Locate every blood parasite and identify its species.
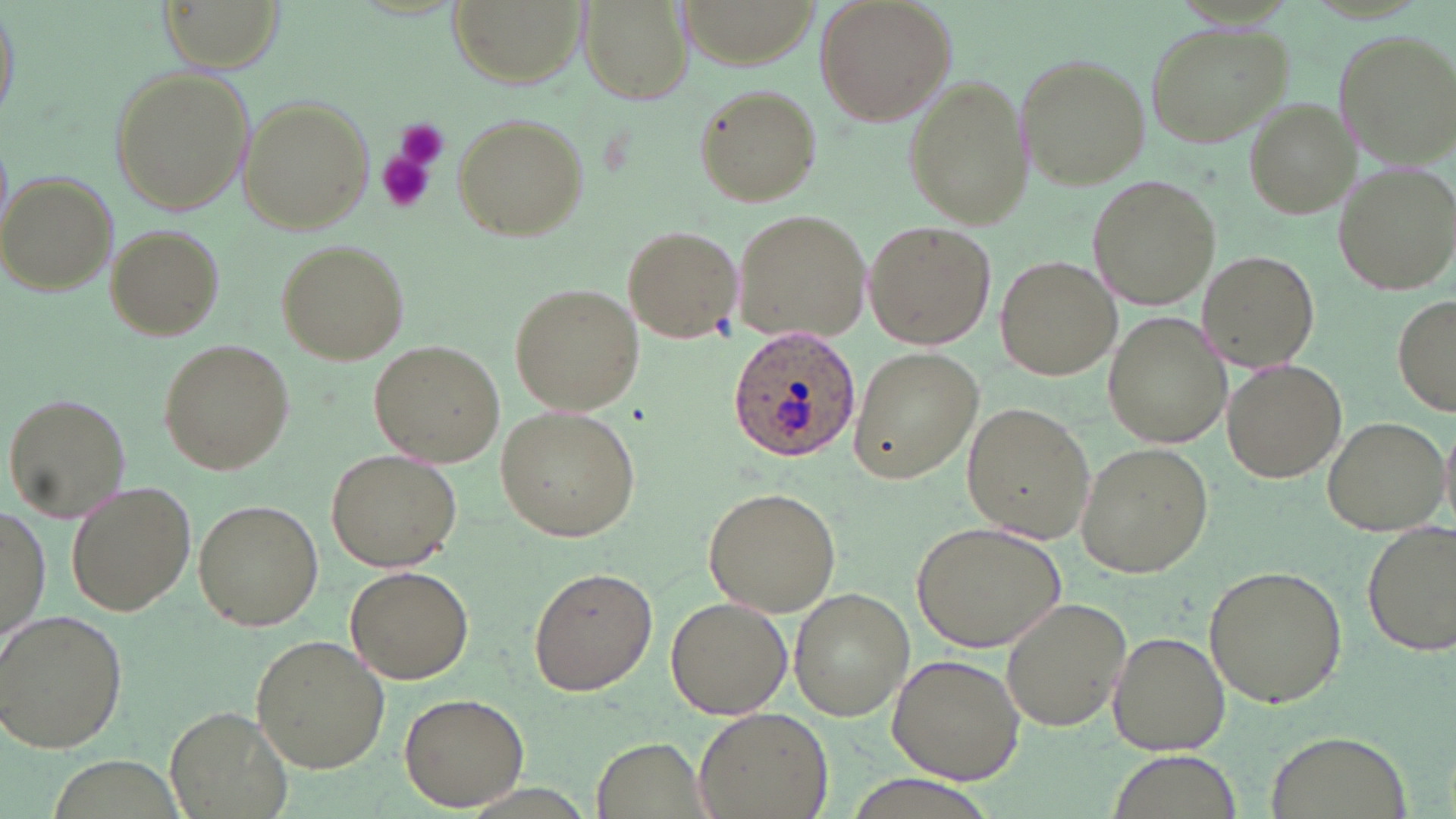
Approximate bounding boxes as [x1, y1, x2, y2] in pixels.
Plasmodium ovale-infected red blood cells: [725, 324, 860, 462].
No Plasmodium falciparum, Plasmodium malariae, Plasmodium vivax, Babesia divergens, or Trypanosoma brucei observed.

Uninfected red blood cell locations: [0, 0, 19, 132], [156, 0, 284, 72], [453, 0, 583, 87], [579, 0, 691, 106], [677, 0, 816, 66], [812, 0, 956, 126], [1145, 22, 1290, 150], [1334, 26, 1456, 164], [1015, 53, 1149, 188], [108, 64, 255, 217], [903, 75, 1030, 229], [692, 83, 823, 207], [237, 96, 373, 234], [1239, 99, 1354, 218], [451, 112, 590, 243], [1333, 162, 1455, 297], [1, 172, 119, 296], [1087, 175, 1217, 310], [731, 207, 873, 347], [863, 221, 994, 352], [622, 223, 742, 342], [105, 224, 222, 338], [275, 239, 409, 366], [1196, 249, 1320, 371], [996, 256, 1122, 381], [510, 282, 643, 415], [1391, 295, 1455, 416], [1103, 310, 1235, 447], [158, 339, 296, 477], [370, 340, 505, 467], [846, 348, 984, 484], [1221, 359, 1346, 483], [5, 393, 130, 521], [962, 400, 1098, 543], [496, 405, 641, 542], [1321, 415, 1448, 537], [1439, 421, 1456, 530], [1074, 442, 1212, 577], [326, 450, 459, 572], [67, 483, 196, 616], [702, 486, 841, 615], [195, 500, 323, 630], [0, 505, 47, 644], [914, 518, 1067, 652], [1361, 519, 1456, 655], [344, 562, 476, 684], [1203, 563, 1350, 709], [527, 565, 657, 695], [788, 589, 913, 721], [665, 595, 790, 719], [998, 597, 1132, 732], [0, 607, 130, 754], [1106, 631, 1230, 756], [249, 634, 389, 772], [887, 650, 1027, 784], [400, 690, 532, 811], [169, 705, 293, 819], [693, 707, 833, 818], [1262, 730, 1413, 819], [591, 738, 711, 818]. Platelet locations: [394, 118, 451, 173], [375, 149, 436, 215]. Slide-level diagnosis: Plasmodium ovale. Light microscopy. Single field of view. Captured at 1000x magnification. May-Grünwald-Giemsa stain. Thin blood smear. Image is 1456×819 pixels.